Name the blood parasite species.
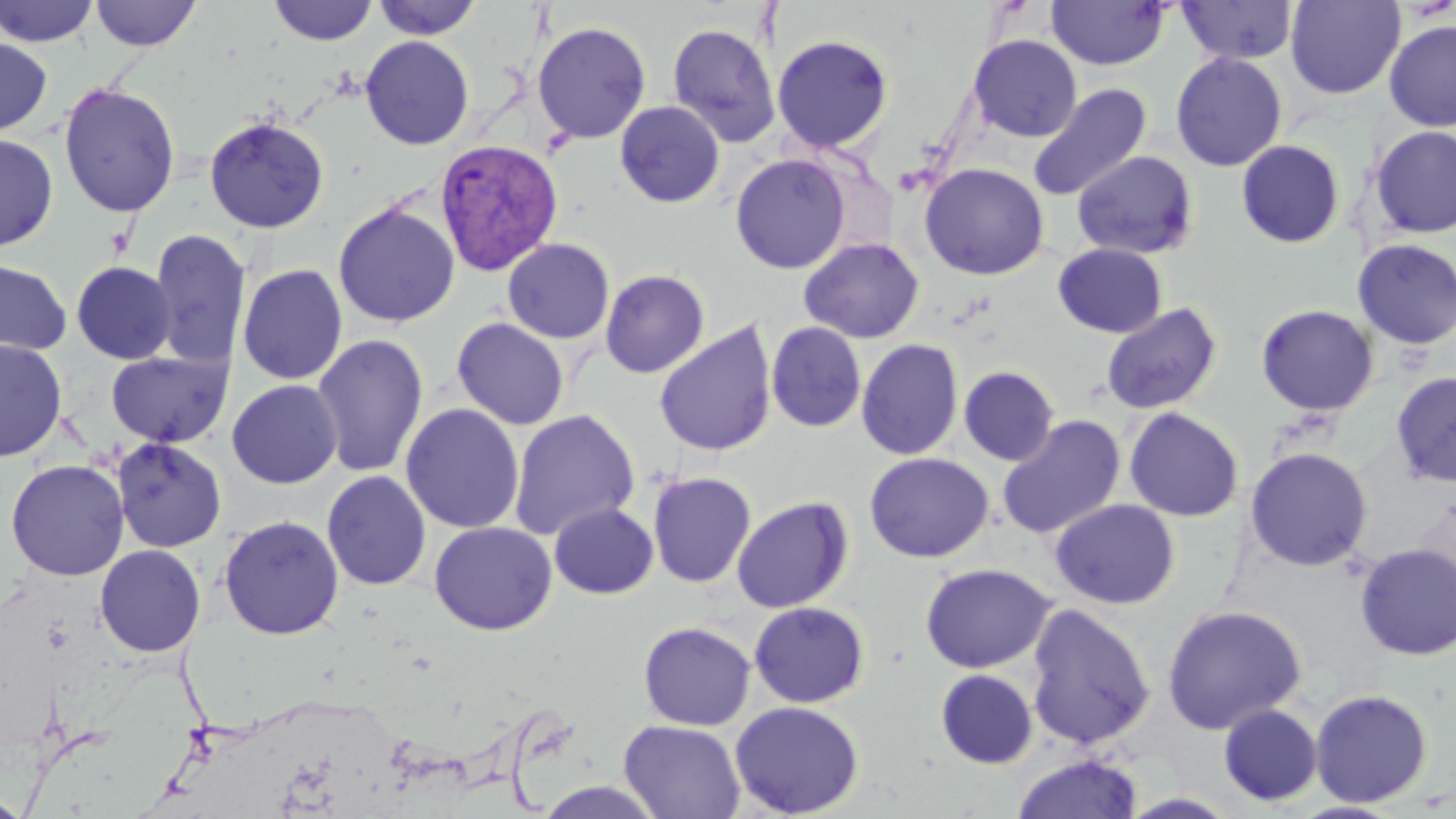

Plasmodium vivax.

Approximate bounding boxes as named x1/y1/x2/y2 corners in pixels. Plasmodium vivax-infected red blood cell locations: (x1=433, y1=138, x2=564, y2=275). Uninfected red blood cell locations: (x1=0, y1=0, x2=100, y2=47), (x1=268, y1=0, x2=379, y2=46), (x1=371, y1=0, x2=483, y2=40), (x1=1046, y1=0, x2=1169, y2=70), (x1=1285, y1=0, x2=1405, y2=99), (x1=89, y1=1, x2=202, y2=52), (x1=1177, y1=1, x2=1298, y2=65), (x1=1383, y1=19, x2=1456, y2=132), (x1=532, y1=21, x2=652, y2=144), (x1=666, y1=21, x2=781, y2=148), (x1=772, y1=34, x2=894, y2=154), (x1=967, y1=34, x2=1082, y2=143), (x1=359, y1=35, x2=474, y2=151), (x1=0, y1=38, x2=53, y2=137), (x1=1170, y1=52, x2=1287, y2=171), (x1=57, y1=81, x2=181, y2=218), (x1=1029, y1=83, x2=1152, y2=200), (x1=614, y1=101, x2=725, y2=208), (x1=203, y1=115, x2=329, y2=234), (x1=1370, y1=125, x2=1456, y2=239), (x1=0, y1=134, x2=58, y2=252), (x1=1236, y1=139, x2=1345, y2=249), (x1=1071, y1=150, x2=1199, y2=260), (x1=730, y1=153, x2=852, y2=275), (x1=919, y1=162, x2=1049, y2=281), (x1=332, y1=201, x2=460, y2=328), (x1=148, y1=228, x2=251, y2=369), (x1=798, y1=237, x2=924, y2=343), (x1=501, y1=238, x2=615, y2=344), (x1=1352, y1=238, x2=1456, y2=350), (x1=1052, y1=243, x2=1168, y2=338), (x1=0, y1=259, x2=72, y2=355), (x1=71, y1=261, x2=177, y2=364), (x1=237, y1=264, x2=348, y2=385), (x1=599, y1=270, x2=710, y2=378), (x1=1100, y1=302, x2=1223, y2=415), (x1=1256, y1=304, x2=1380, y2=417), (x1=451, y1=317, x2=570, y2=430), (x1=654, y1=321, x2=778, y2=457), (x1=766, y1=322, x2=867, y2=433), (x1=311, y1=333, x2=429, y2=479), (x1=0, y1=339, x2=67, y2=461), (x1=856, y1=339, x2=963, y2=461), (x1=106, y1=350, x2=232, y2=448), (x1=958, y1=365, x2=1059, y2=466), (x1=1390, y1=371, x2=1456, y2=487), (x1=227, y1=380, x2=342, y2=489), (x1=400, y1=403, x2=524, y2=534), (x1=1123, y1=406, x2=1245, y2=523), (x1=508, y1=409, x2=640, y2=541), (x1=997, y1=415, x2=1127, y2=540), (x1=112, y1=438, x2=227, y2=553), (x1=1245, y1=446, x2=1374, y2=572), (x1=864, y1=452, x2=994, y2=563), (x1=5, y1=459, x2=130, y2=581), (x1=321, y1=470, x2=432, y2=591), (x1=647, y1=471, x2=757, y2=588), (x1=731, y1=496, x2=853, y2=614), (x1=1050, y1=498, x2=1180, y2=609), (x1=548, y1=502, x2=659, y2=599), (x1=218, y1=515, x2=344, y2=640), (x1=429, y1=521, x2=557, y2=635), (x1=1353, y1=542, x2=1456, y2=661), (x1=94, y1=544, x2=206, y2=657), (x1=919, y1=562, x2=1055, y2=673), (x1=748, y1=601, x2=870, y2=709), (x1=1025, y1=603, x2=1156, y2=750), (x1=1161, y1=604, x2=1307, y2=735), (x1=638, y1=621, x2=756, y2=731), (x1=934, y1=668, x2=1039, y2=770), (x1=1309, y1=688, x2=1434, y2=808), (x1=729, y1=700, x2=865, y2=817), (x1=1217, y1=703, x2=1323, y2=807), (x1=618, y1=719, x2=746, y2=819), (x1=1011, y1=753, x2=1145, y2=819), (x1=0, y1=793, x2=29, y2=818). One field of a larger specimen. Image is 1456×819 pixels. 1000x magnification. May-Grünwald-Giemsa-stained preparation. Optical microscopy. Thin blood film.